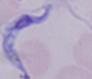

identification = trypanosome
magnification = 1000x
modality = micrograph